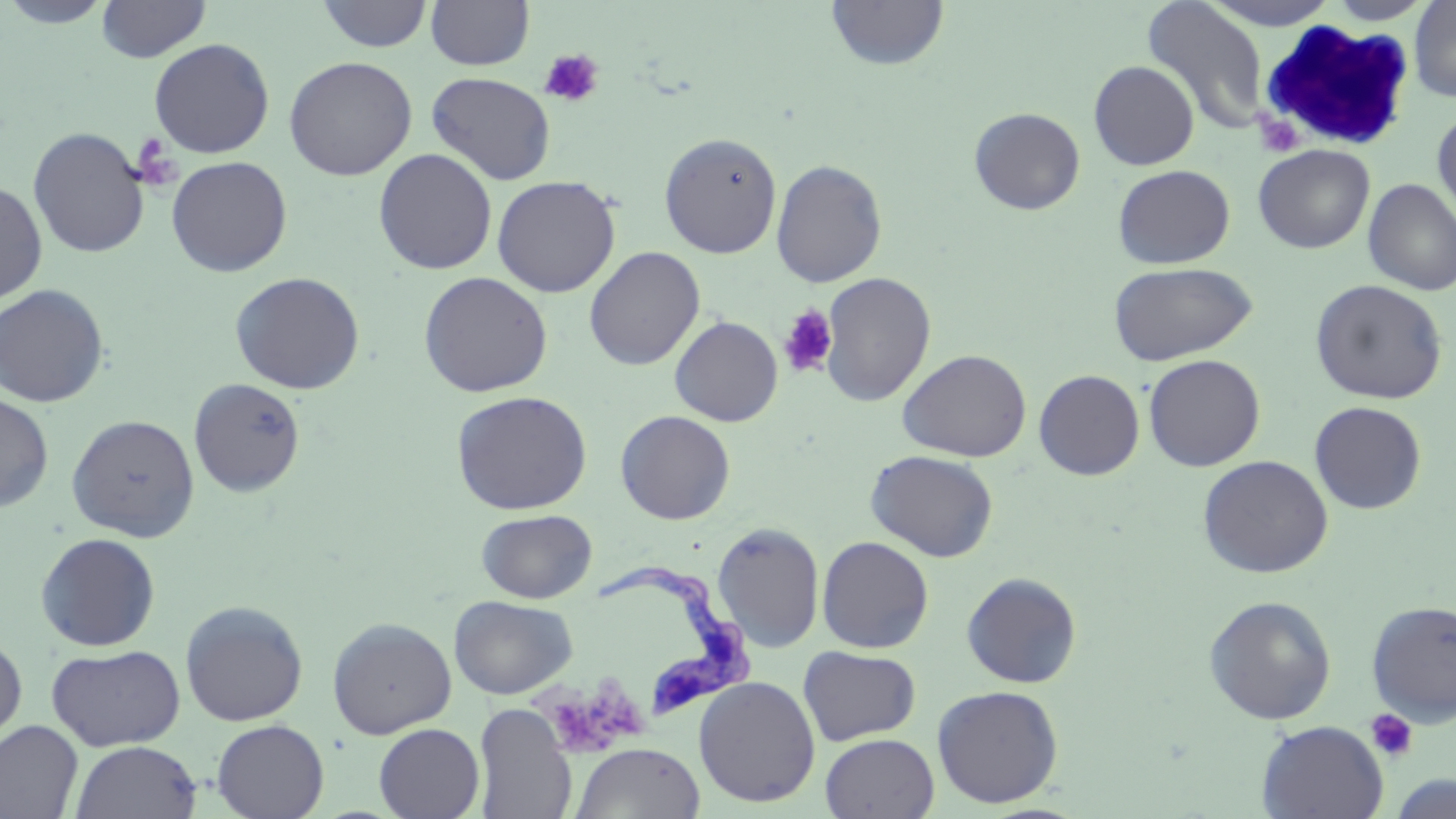
Summary:
  - Coordinate format: approximate bounding boxes as (x1, y1, x2, y2) in pixels
  - Trypanosoma brucei locations: (592, 562, 763, 722)
  - Uninfected red blood cell locations: (0, 0, 116, 28), (96, 0, 211, 62), (425, 0, 535, 70), (826, 0, 949, 71), (1199, 0, 1342, 29), (1322, 0, 1437, 25), (1409, 0, 1456, 102), (315, 1, 434, 52), (1141, 1, 1270, 136), (149, 38, 275, 159), (283, 56, 417, 181), (1088, 61, 1199, 170), (426, 72, 556, 185), (969, 107, 1086, 215), (1432, 107, 1456, 225), (27, 127, 150, 258), (659, 132, 782, 258), (1253, 144, 1375, 253), (373, 148, 497, 274), (166, 156, 292, 277), (771, 159, 888, 288), (1112, 164, 1235, 269), (491, 175, 621, 297), (1362, 178, 1456, 296), (0, 180, 48, 304), (584, 246, 705, 371), (1107, 261, 1258, 366), (229, 271, 365, 394), (418, 271, 553, 398), (819, 271, 936, 407), (1310, 279, 1448, 404), (0, 283, 110, 407), (669, 315, 783, 426), (897, 348, 1032, 462), (1143, 354, 1265, 471), (1034, 369, 1145, 480), (188, 377, 305, 497), (451, 390, 592, 515), (0, 391, 54, 513), (1310, 401, 1427, 514), (615, 410, 736, 524), (66, 413, 200, 542), (865, 449, 998, 562), (1197, 454, 1333, 579), (477, 509, 597, 602), (712, 522, 824, 652), (35, 532, 160, 651), (816, 536, 935, 653), (961, 572, 1082, 688), (448, 595, 578, 699), (1203, 595, 1337, 725), (1366, 599, 1456, 725), (180, 600, 308, 727), (327, 617, 457, 739), (0, 634, 27, 748), (46, 643, 186, 750), (798, 645, 921, 746), (694, 676, 821, 807), (932, 685, 1063, 808), (473, 703, 578, 819), (211, 719, 329, 819), (1257, 720, 1388, 819), (0, 721, 83, 819), (374, 723, 485, 819), (819, 733, 939, 818), (70, 741, 202, 819), (570, 742, 705, 818), (1388, 774, 1455, 819)
  - White blood cell locations: (1256, 19, 1418, 153)
  - Platelet locations: (538, 49, 605, 108), (1253, 112, 1305, 157), (130, 133, 180, 191), (778, 305, 838, 377), (528, 677, 658, 755), (1366, 709, 1419, 762)
  - Slide-level diagnosis: Trypanosoma brucei
  - Image size: 1456×819 pixels
  - Field of view: one of a larger specimen
  - Modality: light microscopy
  - Stain: May-Grünwald-Giemsa
  - Magnification: 1000x
  - Preparation: thin blood film